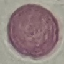

Summary:
  - Malaria status: uninfected
  - Capture: smartphone camera at the microscope eyepiece
  - Image type: automatically extracted cell patch, resized to 64 × 64 pixels
  - Stain: Giemsa
  - Preparation: thin blood smear